Point out leukocytes.
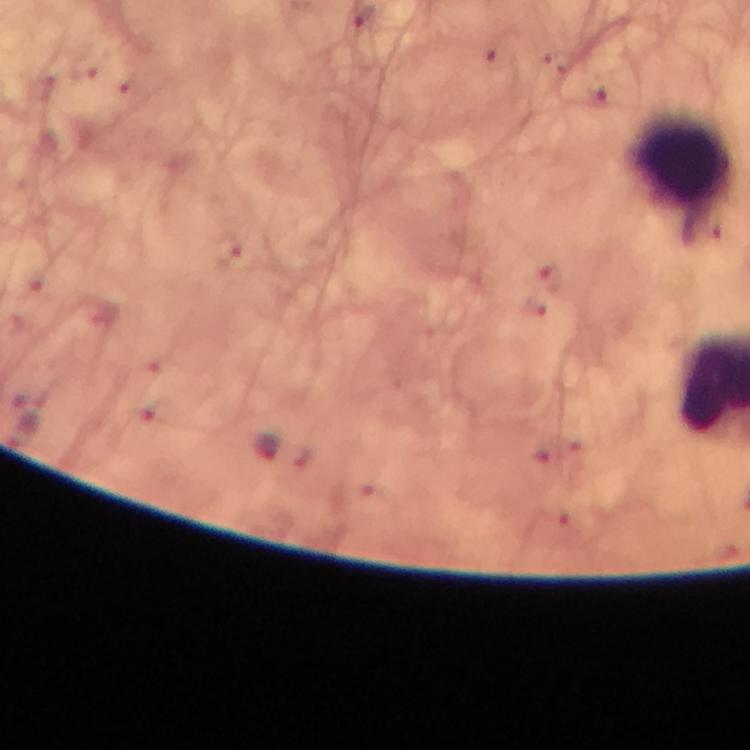

Approximate centers as (x, y) in pixels.
Leukocytes: (680, 159).

From a diagnostic examination for malaria. Thick blood smear. Image is 750×750 pixels. Giemsa-stained preparation. Photographed with a smartphone mounted on the microscope. Immersion oil was used. A crop from one field of view. Malaria parasites: none detected. At 100x magnification.